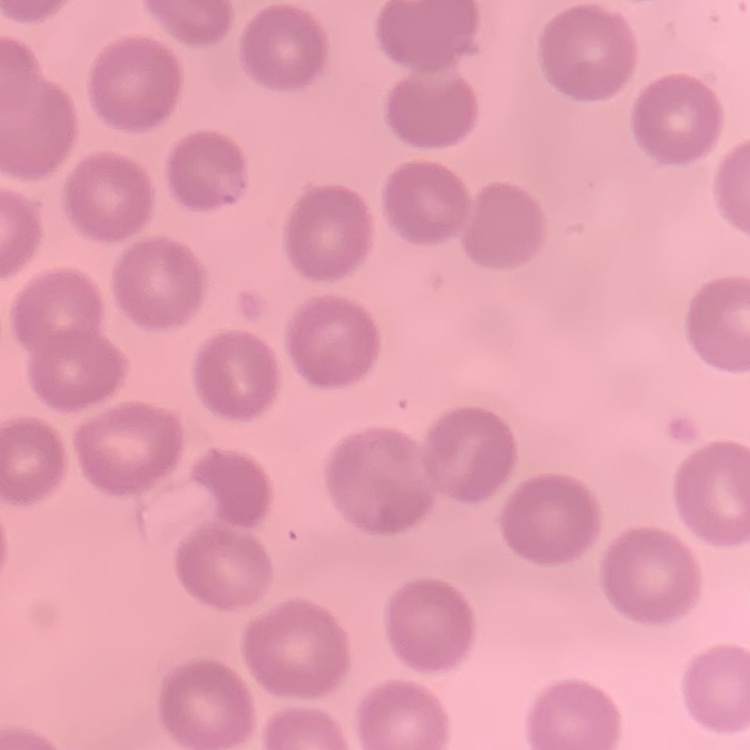

erythrocyte morphology = no rouleaux formation
image type = one tile cut from a larger photomicrograph
preparation = thin blood smear
stain = Field's or Giemsa